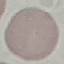
result: negative for malaria parasites
capture: smartphone through the microscope eyepiece
preparation: thin blood film
image_type: automatically extracted cell patch, resized to 64 × 64 pixels
stain: Giemsa